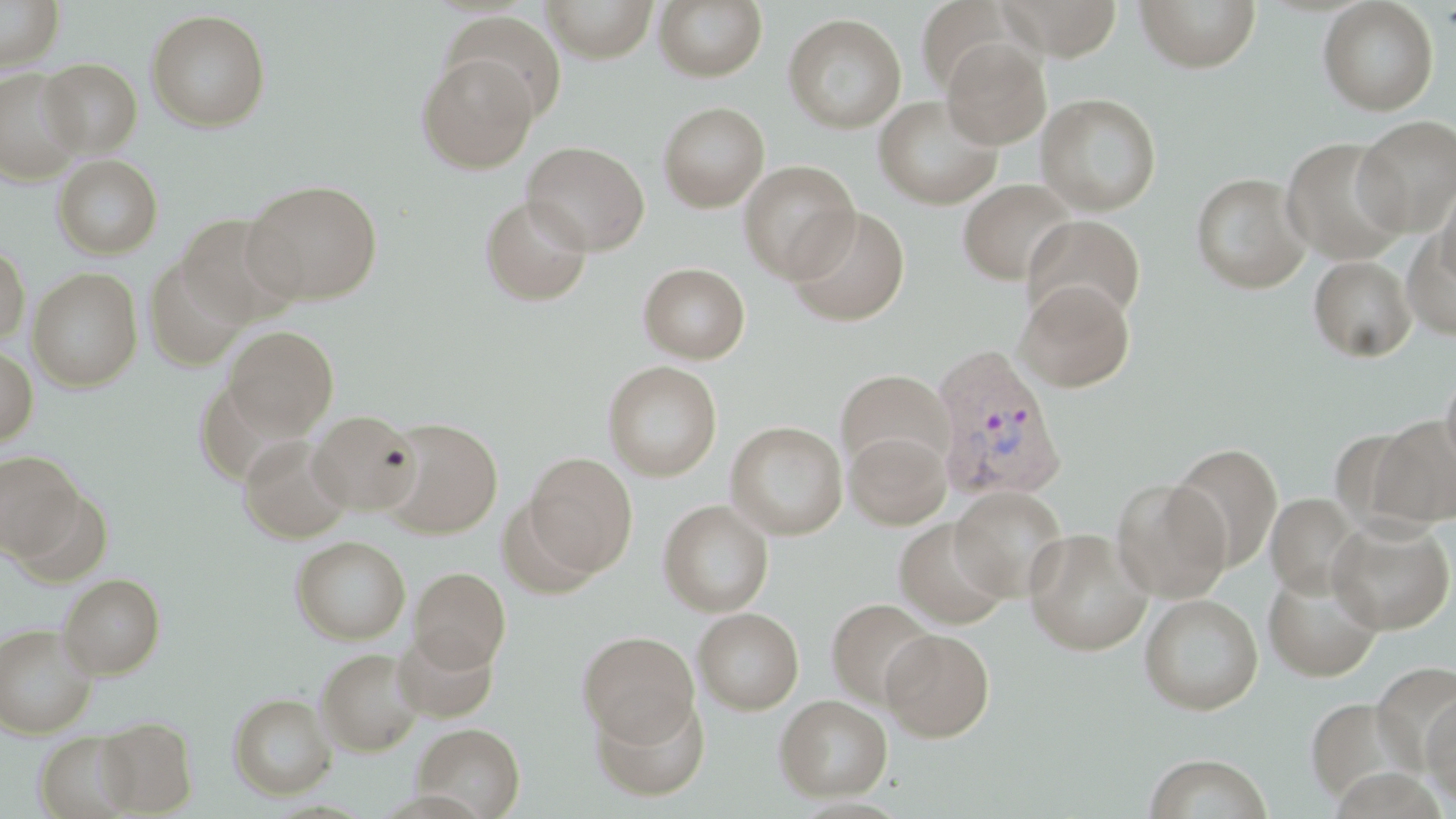

slide_level_diagnosis: Plasmodium vivax
stain: May-Grünwald-Giemsa
uninfected_red_blood_cell_locations: 'approximate bounding boxes as (x1,y1)-(x2,y2) corner pairs in pixels: (0,0)-(65,72), (542,0)-(658,61), (654,0)-(767,81), (1134,0)-(1261,73), (1317,0)-(1439,115), (997,1)-(1124,59), (146,9)-(271,132), (441,12)-(568,124), (783,12)-(907,134), (940,37)-(1051,149), (417,53)-(539,174), (39,58)-(143,157), (0,67)-(84,185), (1036,92)-(1162,216), (873,94)-(1003,209), (658,101)-(770,212), (1354,116)-(1456,236), (1280,136)-(1410,265), (522,141)-(650,255), (53,154)-(163,259), (738,159)-(859,283), (1190,172)-(1312,293), (243,179)-(383,305), (957,179)-(1077,286), (1435,179)-(1456,291), (480,195)-(592,306), (786,205)-(912,327), (177,212)-(299,327), (1023,215)-(1146,327), (1401,229)-(1456,342), (0,244)-(30,345), (1308,254)-(1417,363), (144,255)-(250,371), (638,262)-(750,364), (28,267)-(142,391), (1015,279)-(1136,393), (223,325)-(339,438), (0,345)-(37,446), (603,361)-(722,481), (835,369)-(954,478), (1441,369)-(1456,472), (308,410)-(422,514), (1369,415)-(1456,527), (378,417)-(502,538), (725,420)-(848,540), (844,429)-(951,529), (238,434)-(353,544), (1167,441)-(1284,572), (0,451)-(84,560), (524,452)-(638,577), (1109,477)-(1232,602), (949,485)-(1069,602), (1266,493)-(1362,598), (658,499)-(774,617), (893,517)-(1011,630), (1328,517)-(1455,634), (1023,529)-(1154,656), (291,535)-(411,644), (1263,565)-(1383,682), (410,567)-(510,672), (58,573)-(165,678), (1139,593)-(1263,715), (826,598)-(937,709), (694,607)-(804,714), (0,623)-(99,739), (394,627)-(500,722), (881,629)-(994,741), (577,630)-(700,745), (315,648)-(424,756), (1419,690)-(1456,805), (591,691)-(710,801), (228,692)-(336,799), (775,695)-(892,801), (1304,695)-(1421,804), (95,716)-(198,816), (412,722)-(525,818), (34,731)-(138,819), (1142,753)-(1272,819)'
plasmodium_vivax_infected_red_blood_cell_locations: 'approximate bounding boxes as (x1,y1)-(x2,y2) corner pairs in pixels: (930,345)-(1066,503)'
magnification: 1000x
preparation: thin blood film
field_of_view: single
modality: optical microscopy
image_size: 1456×819 pixels